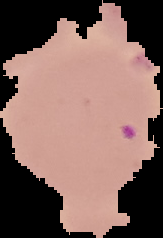

Summary:
  - Preparation: thin blood film
  - Image type: segmented cell region with the area outside set to black
  - Result: Plasmodium parasites detected
  - Image size: 163×238 pixels